Assess this cell for malaria.
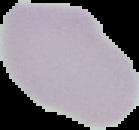

It is uninfected.

{
  "preparation": "thin blood film",
  "image_type": "segmented cell region on a black background",
  "image_size": "139×130 pixels"
}